Classify this cell by malaria status.
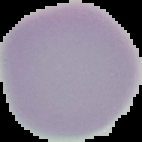

Uninfected.

Image is 142×142 pixels. From a thin blood film. Cell region segmented out of the field of view; the surrounding area is masked to black.